Give the extent of all Babesia divergens-infected red blood cells.
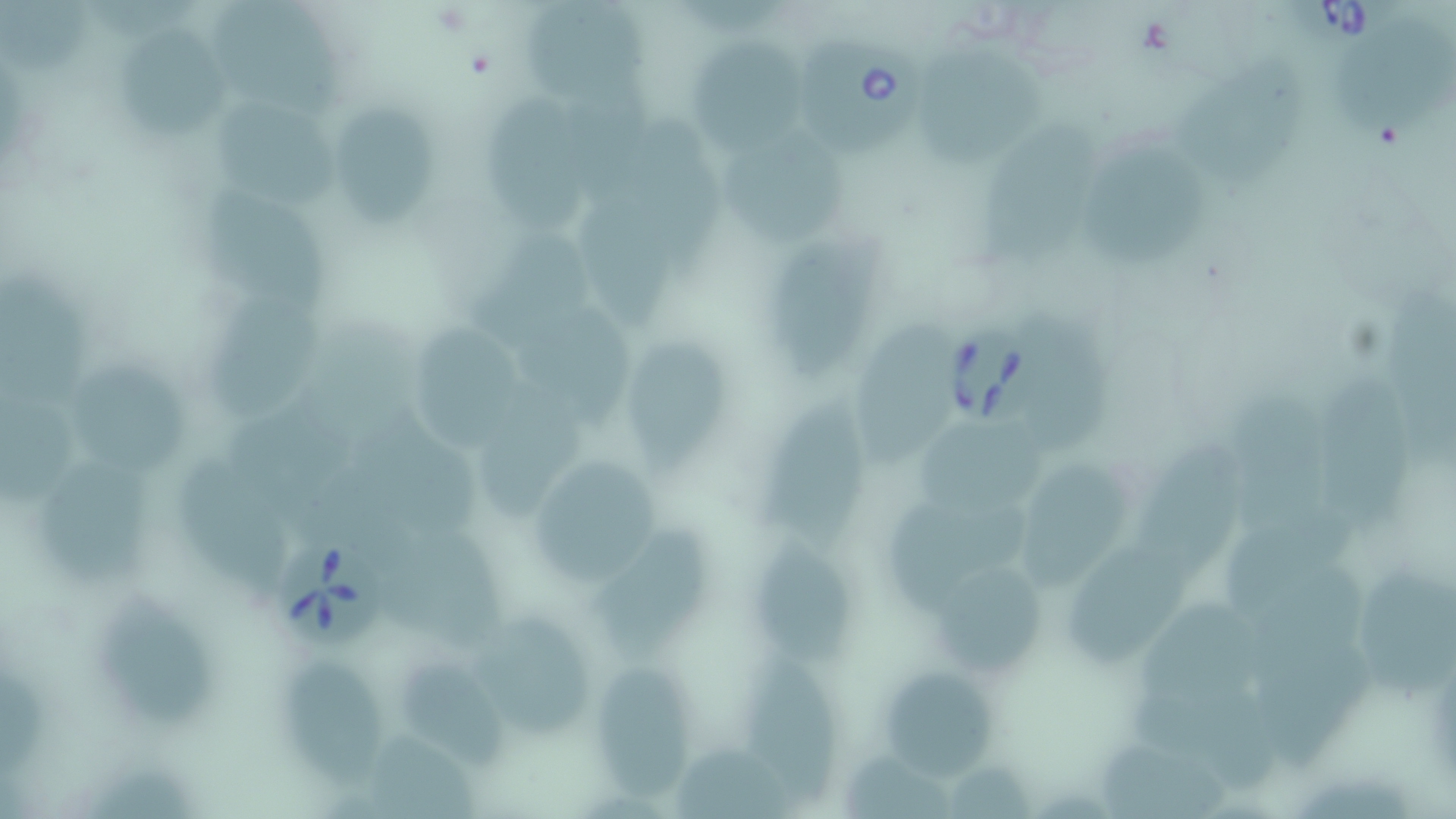

Approximate bounding boxes as (x1,y1)-(x2,y2) corner pairs in pixels.
Babesia divergens-infected red blood cells: (1287,0)-(1410,47), (796,37)-(932,162), (942,323)-(1050,430), (281,540)-(383,651).

slide-level diagnosis = Babesia divergens
field of view = one of a larger specimen
image size = 1456×819 pixels
modality = light microscopy
preparation = thin blood smear
magnification = 1000x
stain = May-Grünwald-Giemsa
uninfected red blood cell locations = approximate bounding boxes as (x1,y1)-(x2,y2) corner pairs in pixels: (1,0)-(93,75), (210,0)-(349,117), (521,4)-(657,111), (121,22)-(229,139), (1331,23)-(1448,139), (687,32)-(816,154), (918,49)-(1047,169), (1168,52)-(1307,184), (570,56)-(656,212), (480,88)-(593,240), (216,98)-(346,216), (333,108)-(440,230), (967,112)-(1114,267), (718,130)-(845,244), (1084,135)-(1217,267), (203,184)-(339,306), (582,209)-(678,330), (485,222)-(595,338), (770,235)-(881,379), (0,271)-(102,403), (203,286)-(324,423), (525,305)-(639,438), (856,311)-(965,472), (1028,313)-(1118,456), (412,321)-(522,455), (627,335)-(729,477), (71,357)-(191,480), (1321,362)-(1422,530), (477,377)-(593,519), (758,388)-(872,552), (1229,392)-(1341,526), (0,394)-(85,504), (225,395)-(362,513), (356,414)-(489,534), (920,422)-(1059,516), (1131,423)-(1248,581), (521,449)-(670,595), (179,452)-(291,596), (36,464)-(148,585), (1020,464)-(1124,586), (888,495)-(1029,604), (1225,508)-(1356,612), (598,522)-(711,660), (383,528)-(506,642), (749,533)-(853,666), (1071,536)-(1196,673), (939,561)-(1042,676), (1354,564)-(1456,696), (99,582)-(218,730), (1142,603)-(1255,703), (475,612)-(595,739), (1260,639)-(1381,766), (395,645)-(506,772), (283,653)-(377,792), (758,653)-(839,800), (881,668)-(1004,783), (596,669)-(692,804), (1135,681)-(1284,799), (679,737)-(803,819), (1090,739)-(1231,819), (843,746)-(954,819)